State which cell type is depicted.
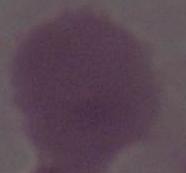
This is an erythrocyte.

{
  "modality": "photomicrograph",
  "magnification": "1000x"
}